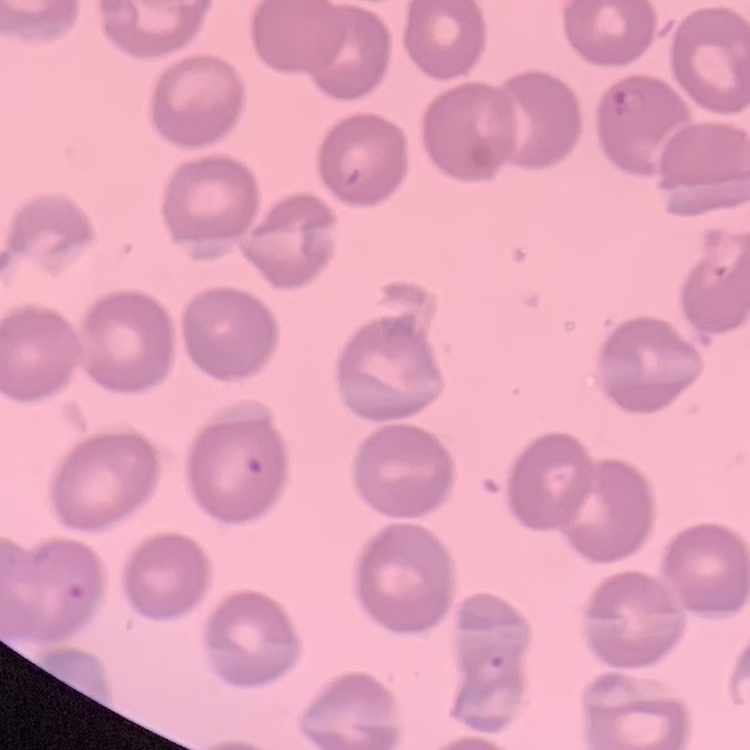
Summary:
  - Erythrocyte morphology: no rouleaux formation
  - Preparation: thin peripheral smear
  - Image type: square crop of a larger photomicrograph
  - Stain: Field's or Giemsa